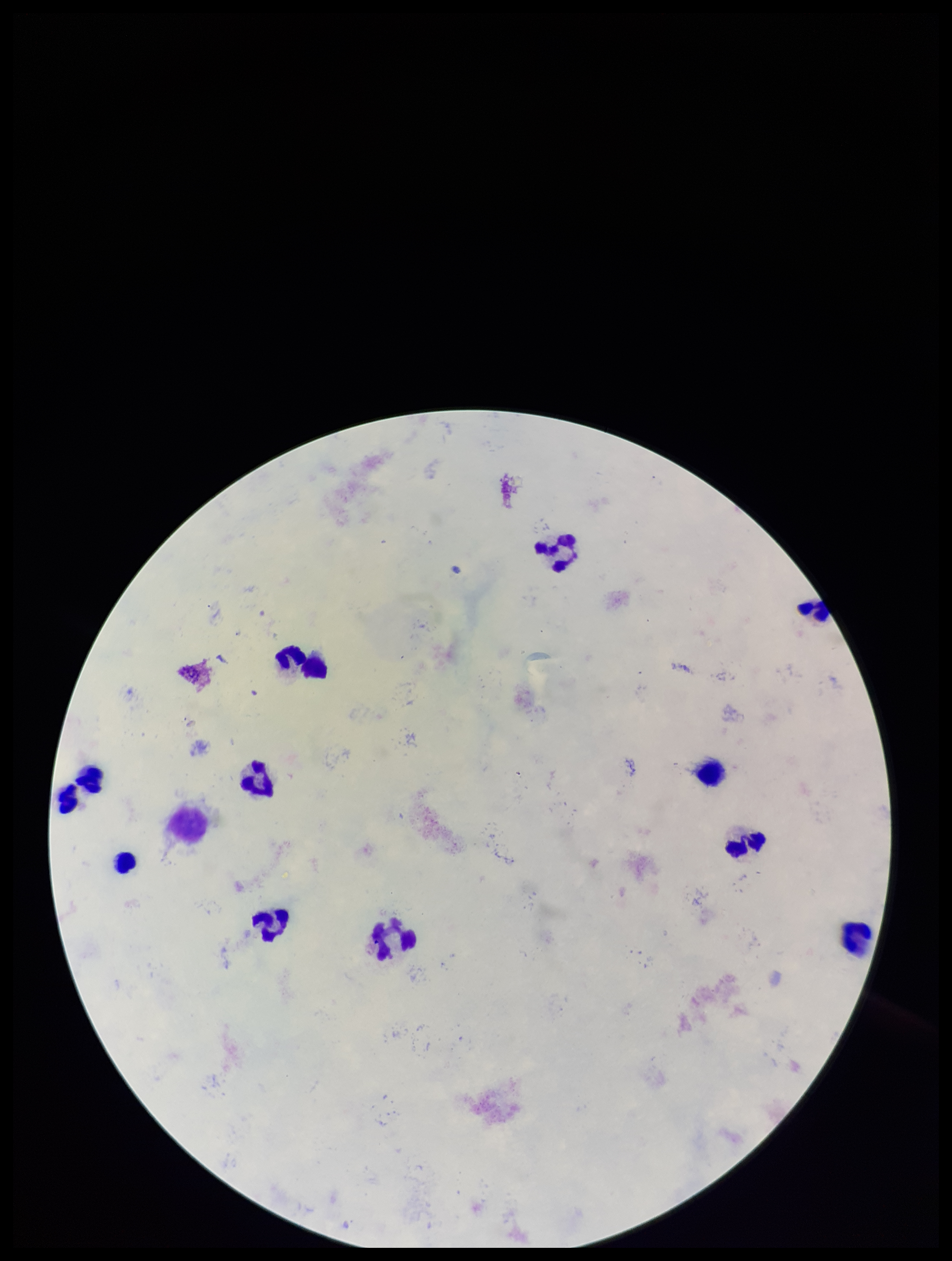
field of view = single
patient malaria status = negative
parasite count = 0
capture = smartphone photograph through the microscope eyepiece
preparation = thick
leukocyte count = 11
stain = Giemsa
image size = 952×1261 pixels
Plasmodium parasites = none identified